Classify this cell by malaria status.
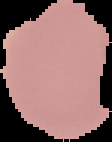
Uninfected.

Summary:
  - Image type: segmented cell region with the area outside set to black
  - Image size: 112×142 pixels
  - Preparation: thin blood film